Comment on the morphology of the red blood cells.
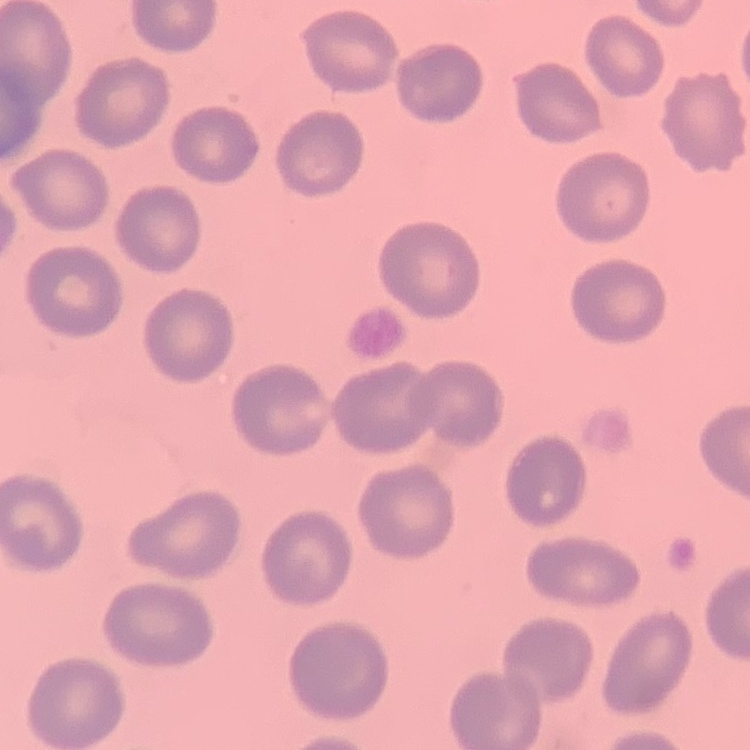
They show no rouleaux formation.

{
  "preparation": "thin blood film",
  "stain": "Field's or Giemsa",
  "image_type": "one tile cut from a larger photomicrograph"
}